State which parasite is depicted.
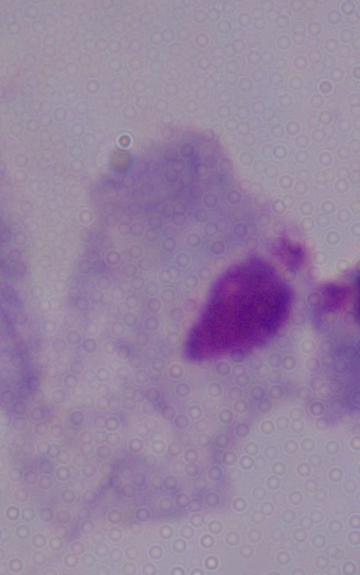
This is a trichomonad.

Micrograph. Captured at 1000x magnification.